Classify this cell by malaria status.
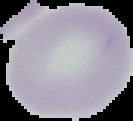
It is uninfected.

Cell region segmented out of the field of view; the surrounding area is masked to black. Image is 133×121 pixels. From a thin blood film.